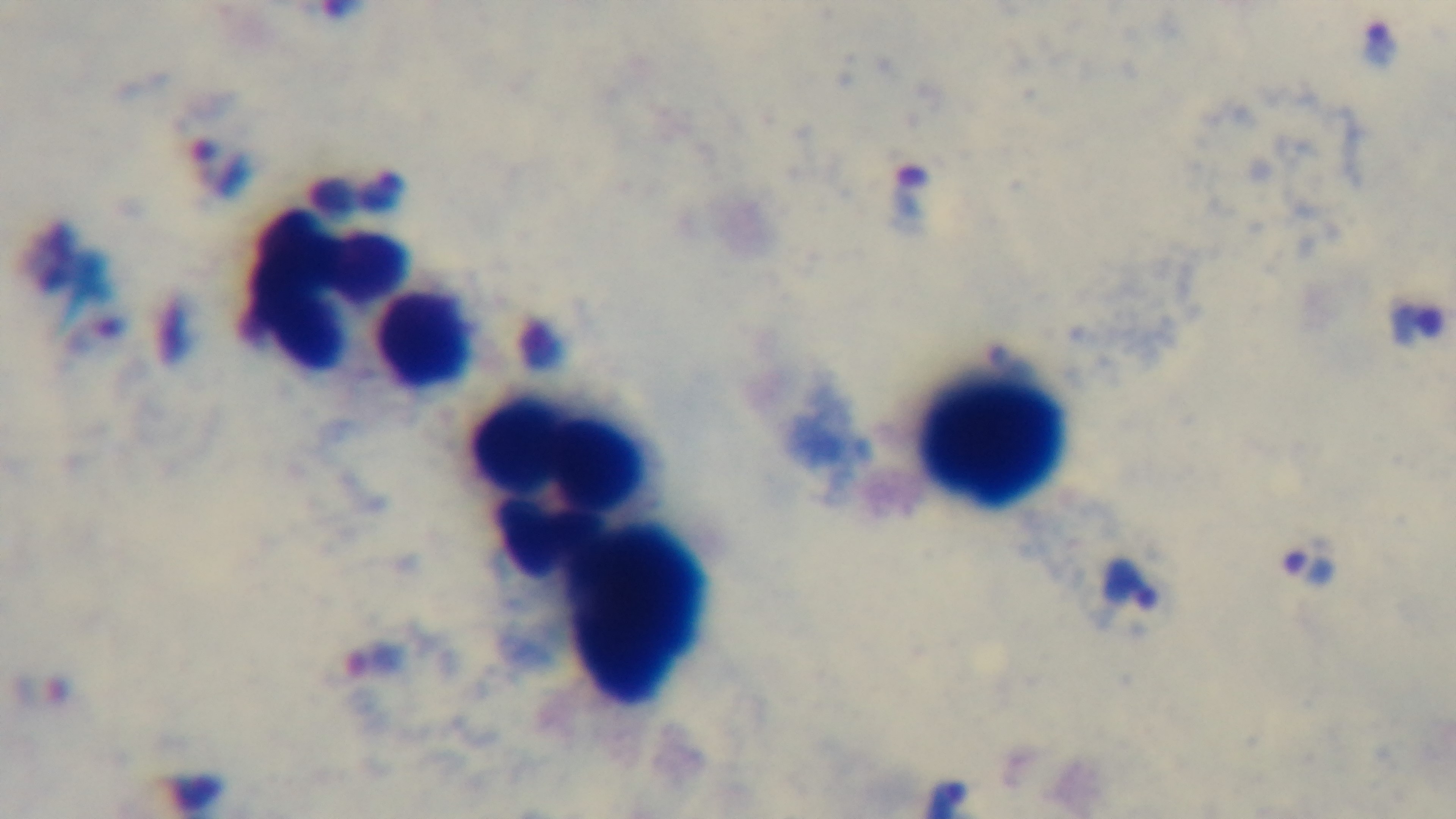

Summary:
  - Objective: 100x oil immersion
  - Stain: Giemsa
  - Field of view: single
  - Capture: mounted 4K digital camera
  - Malaria status: positive
  - Modality: light microscopy
  - Preparation: thick